Assess this cell for malaria.
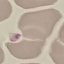
Uninfected.

{
  "capture": "smartphone through the microscope eyepiece",
  "image_type": "automatically extracted cell patch, resized to 64 × 64 pixels",
  "stain": "Giemsa",
  "preparation": "thin blood film"
}